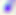
identification = Toxoplasma gondii
magnification = 400x
modality = photomicrograph